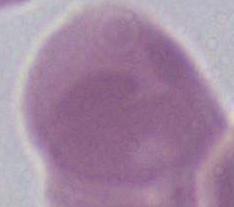 An erythrocyte is shown. 1000x magnification. Micrograph.